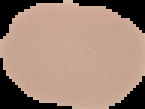
image type = cell region segmented out of the field of view; surrounding area masked to black
preparation = thin blood film
result = negative for Plasmodium parasites
image size = 145×109 pixels